Assess this cell for malaria.
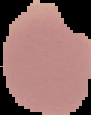
It is uninfected.

Image is 91×115 pixels. From a thin blood smear. The area outside the segmented cell region is set to black.